Outline each uninfected red blood cell.
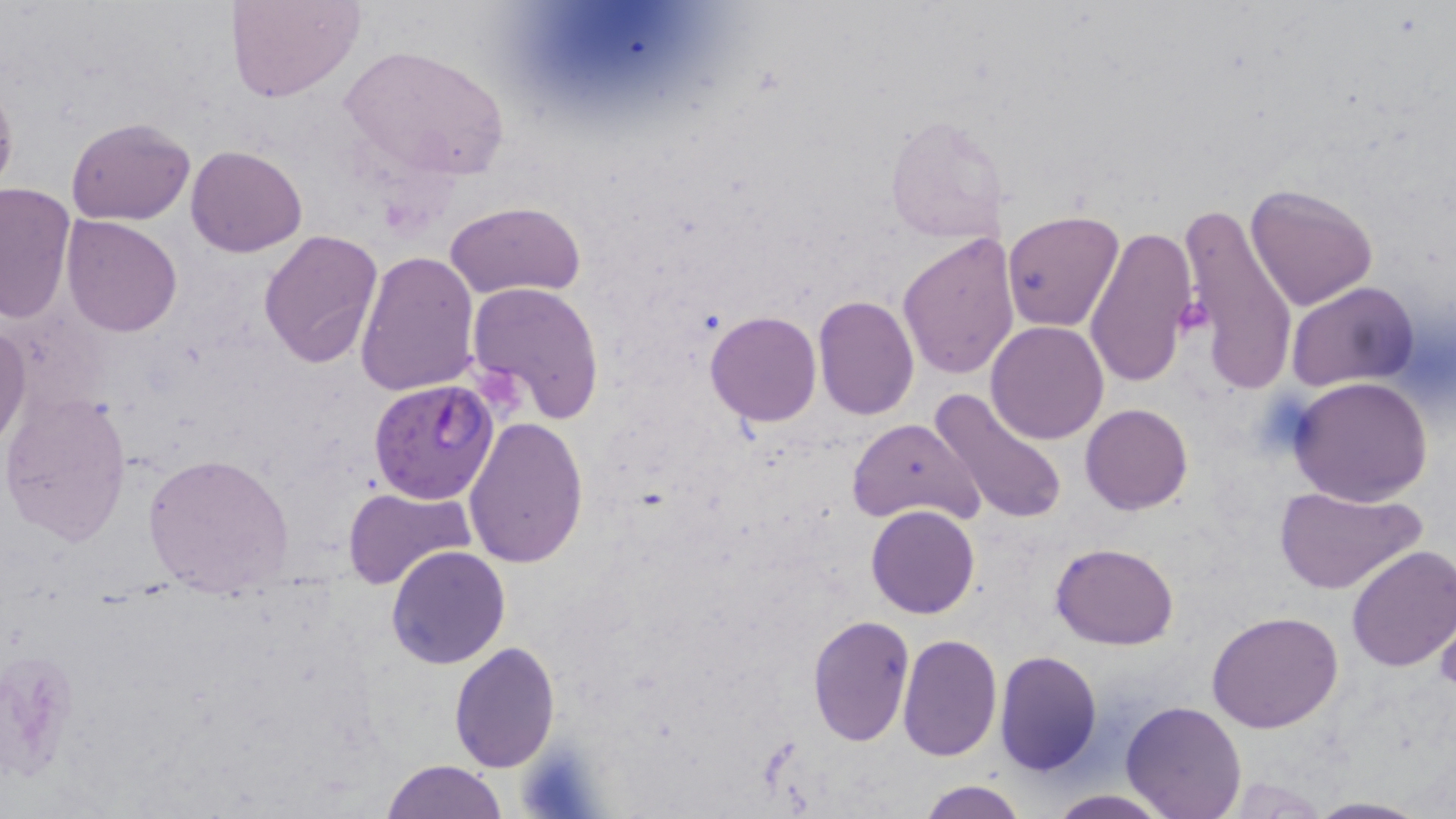

Approximate bounding boxes as (x1,y1)-(x2,y2) corner pairs in pixels.
Uninfected red blood cells: (228,0)-(365,104), (339,46)-(508,181), (0,79)-(18,201), (884,113)-(1009,243), (65,115)-(196,224), (185,144)-(307,257), (1245,183)-(1377,311), (0,184)-(75,324), (445,201)-(589,302), (1178,204)-(1301,390), (1000,210)-(1123,331), (61,216)-(182,336), (1085,224)-(1199,388), (257,228)-(383,369), (896,233)-(1020,381), (354,250)-(480,397), (467,280)-(605,422), (1285,281)-(1418,392), (813,295)-(919,421), (703,311)-(821,427), (986,321)-(1111,444), (0,326)-(30,448), (1290,376)-(1433,506), (929,384)-(1067,525), (0,390)-(134,547), (1079,403)-(1193,515), (463,415)-(589,568), (848,415)-(982,528), (142,452)-(295,593), (1273,482)-(1426,594), (343,487)-(475,592), (1298,504)-(1456,644), (867,505)-(980,618), (1050,541)-(1178,650), (386,544)-(511,667), (1346,545)-(1456,672), (1207,609)-(1345,733), (806,615)-(914,745), (1435,618)-(1456,694), (898,632)-(1003,760), (448,640)-(560,772), (994,650)-(1102,776), (1122,701)-(1246,819), (382,759)-(507,818), (915,779)-(1030,819), (1042,789)-(1176,819), (1306,796)-(1429,817).

Summary:
  - Plasmodium falciparum-infected red blood cell locations: (368,377)-(500,504)
  - Platelet locations: (1175,294)-(1213,342), (521,739)-(603,819)
  - Slide-level diagnosis: Plasmodium falciparum
  - Image size: 1456×819 pixels
  - Modality: optical microscopy
  - Preparation: thin blood smear
  - Stain: May-Grünwald-Giemsa
  - Magnification: 1000x
  - Field of view: one of a larger specimen